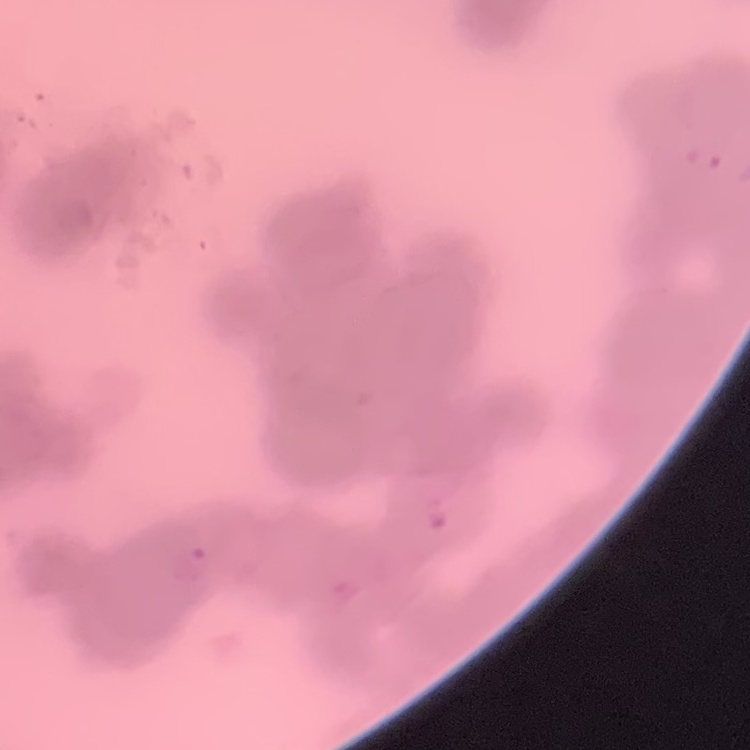

Summary:
  - Red blood cell morphology: rouleaux formation
  - Stain: Field's or Giemsa
  - Image type: one tile cut from a larger photomicrograph
  - Preparation: thin blood film